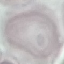

{
  "result": "no malaria parasites detected",
  "image_type": "automatically extracted cell patch, resized to 64 × 64 pixels",
  "stain": "Giemsa",
  "capture": "smartphone camera at the microscope eyepiece",
  "preparation": "thin blood film"
}